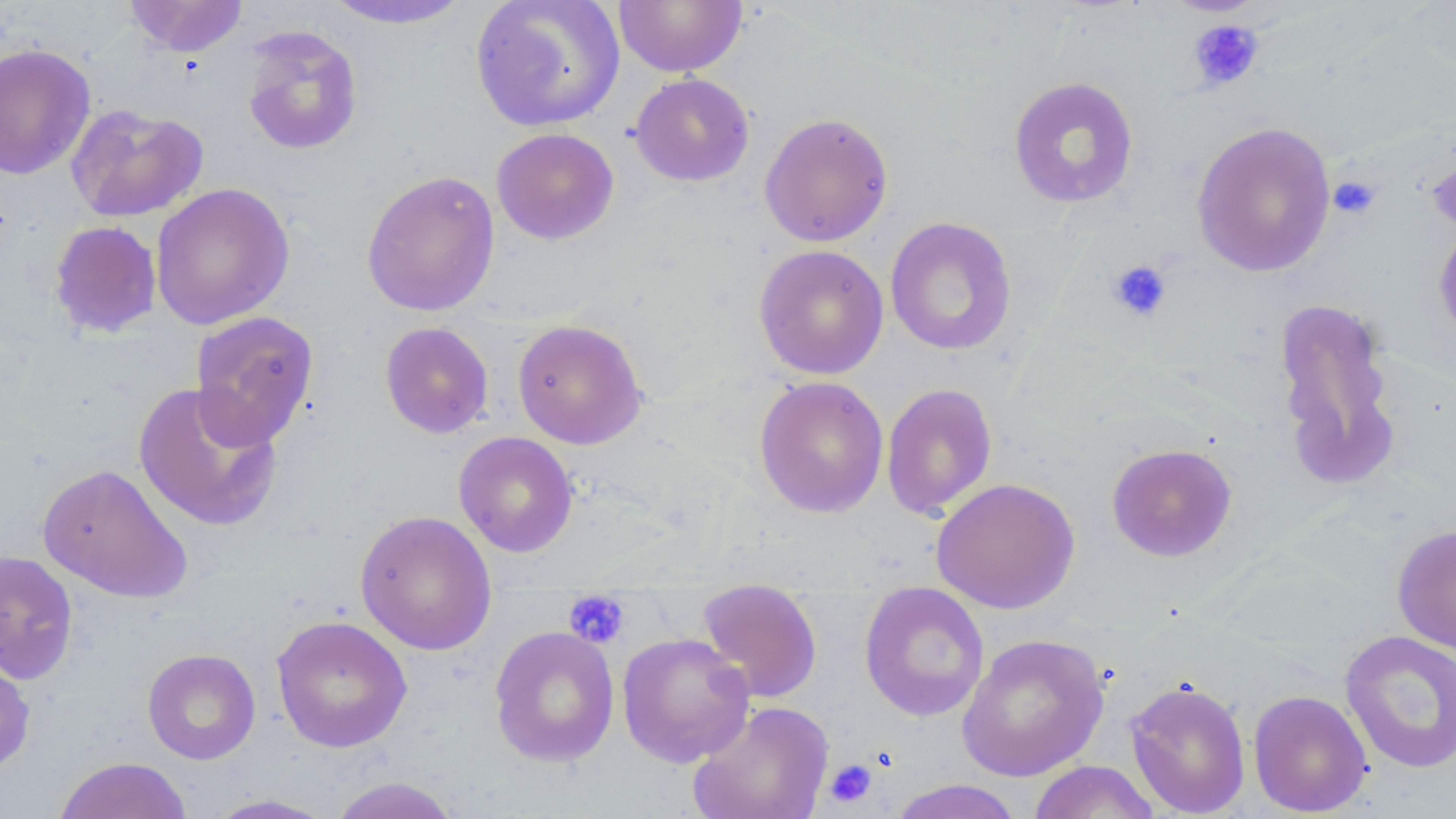
Approximate bounding boxes as (x1,y1)-(x2,y2) corner pairs in pixels. Platelet locations: (1187,18)-(1265,91), (1327,174)-(1382,220), (1106,259)-(1173,323), (563,591)-(630,649), (825,758)-(878,808). Uninfected red blood cell locations: (125,0)-(248,57), (470,0)-(625,132), (319,1)-(477,30), (613,1)-(747,76), (240,25)-(363,156), (0,43)-(97,180), (629,73)-(755,187), (1008,75)-(1140,209), (66,103)-(208,223), (759,112)-(894,247), (1191,121)-(1336,277), (491,127)-(619,244), (1425,140)-(1456,240), (361,169)-(500,317), (150,183)-(294,331), (884,217)-(1018,356), (48,220)-(163,339), (1432,220)-(1456,344), (753,244)-(889,380), (1272,296)-(1402,490), (189,310)-(319,449), (512,318)-(648,449), (379,321)-(494,438), (753,375)-(889,518), (132,382)-(285,532), (881,383)-(998,519), (453,431)-(579,557), (1105,443)-(1239,563), (37,463)-(193,603), (931,477)-(1080,614), (354,509)-(497,656), (1391,523)-(1456,654), (0,549)-(79,684), (859,583)-(990,722), (696,589)-(822,703), (270,615)-(413,753), (489,625)-(620,767), (1339,629)-(1456,775), (617,632)-(755,768), (956,632)-(1110,781), (0,648)-(36,778), (142,648)-(261,764), (1124,678)-(1251,817), (1248,689)-(1372,817), (688,700)-(834,819), (54,756)-(194,819), (1027,760)-(1162,819), (327,776)-(462,819), (887,779)-(1024,819), (206,794)-(337,818). Slide-level diagnosis: negative for blood parasites. 1000x magnification. Thin blood smear. Single field of view. May-Grünwald-Giemsa-stained preparation. Image is 1456×819 pixels. Optical microscopy.